Identify the blood parasite species.
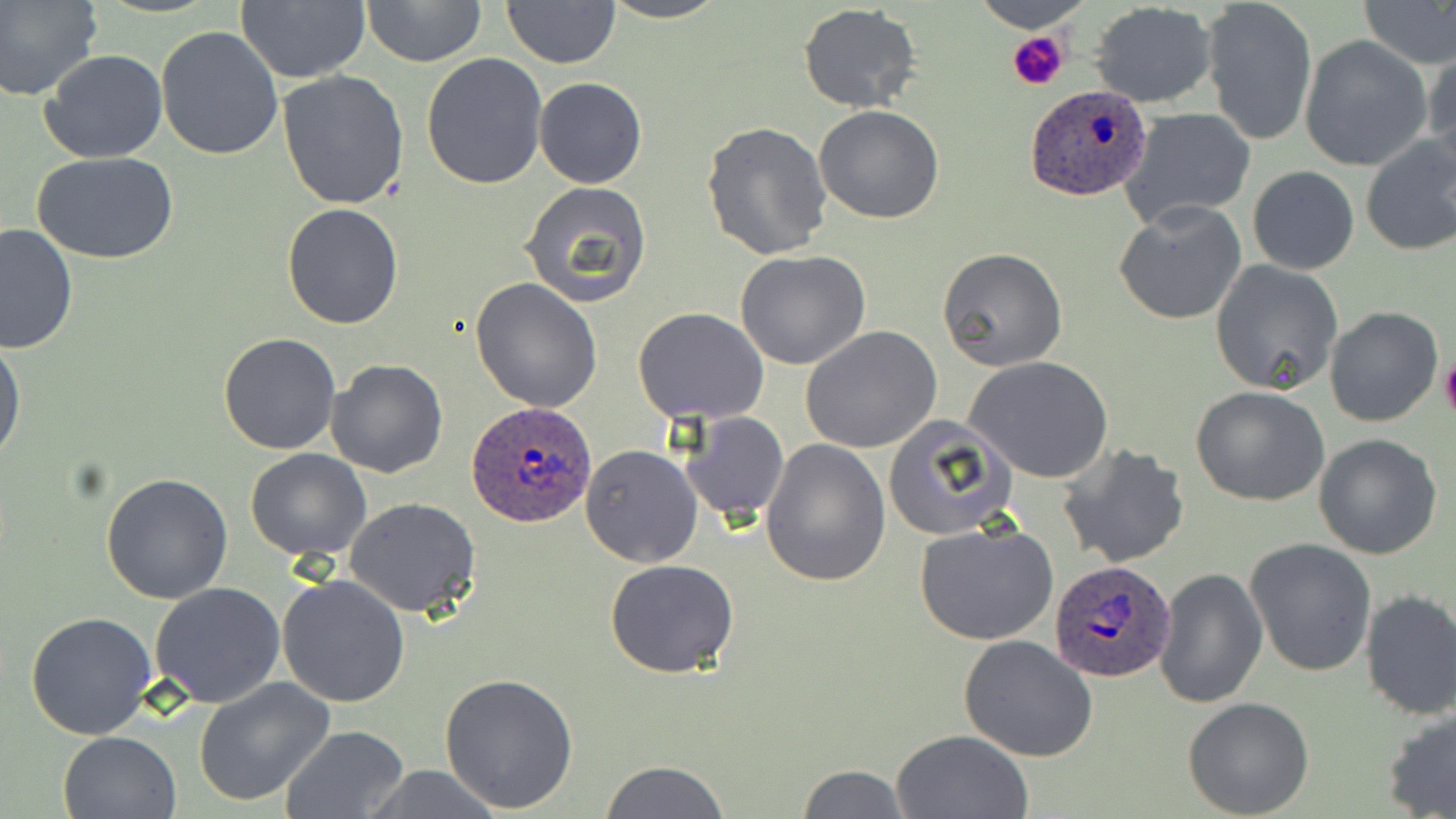
Plasmodium ovale.

Summary:
  - Coordinate format: approximate bounding boxes as (x1, y1, x2, y2) in pixels
  - Platelet locations: (1007, 32, 1071, 91), (1440, 359, 1456, 419)
  - Plasmodium ovale-infected red blood cell locations: (1025, 82, 1153, 199), (468, 401, 596, 528), (1050, 558, 1177, 683)
  - Uninfected red blood cell locations: (0, 0, 101, 102), (236, 0, 370, 84), (500, 0, 619, 68), (598, 0, 731, 24), (969, 0, 1095, 34), (1201, 0, 1317, 145), (362, 1, 486, 67), (1358, 1, 1456, 69), (1090, 2, 1216, 108), (797, 3, 923, 114), (155, 25, 285, 160), (1299, 36, 1433, 170), (40, 48, 168, 164), (1424, 49, 1456, 179), (421, 53, 548, 191), (278, 69, 410, 210), (534, 77, 646, 189), (814, 105, 946, 223), (1119, 108, 1257, 230), (701, 122, 832, 259), (1359, 135, 1456, 257), (32, 151, 180, 265), (1247, 164, 1359, 275), (519, 181, 653, 307), (1114, 201, 1247, 325), (281, 203, 405, 328), (1, 221, 78, 356), (938, 246, 1069, 372), (736, 249, 872, 369), (1211, 259, 1344, 396), (470, 277, 605, 412), (632, 306, 769, 425), (1323, 307, 1444, 428), (800, 326, 942, 453), (1, 331, 26, 471), (218, 333, 342, 454), (968, 357, 1113, 483), (325, 358, 449, 476), (1190, 385, 1330, 507), (678, 409, 789, 523), (883, 413, 1016, 542), (1313, 433, 1443, 558), (761, 438, 891, 585), (1058, 443, 1190, 569), (580, 445, 703, 567), (246, 449, 372, 561), (101, 473, 233, 604), (343, 497, 482, 620), (914, 519, 1060, 647), (1245, 538, 1378, 678), (605, 560, 739, 679), (1153, 568, 1267, 708), (277, 574, 411, 707), (150, 582, 286, 708), (1359, 588, 1456, 719), (26, 610, 158, 740), (958, 632, 1100, 761), (439, 672, 581, 814), (193, 677, 335, 807), (1182, 697, 1314, 818), (1380, 706, 1456, 818), (281, 725, 410, 819), (891, 729, 1033, 818), (57, 730, 182, 819), (602, 760, 730, 818), (795, 764, 910, 818), (355, 766, 509, 818)
  - Magnification: 1000x
  - Image size: 1456×819 pixels
  - Stain: May-Grünwald-Giemsa
  - Preparation: thin blood smear
  - Field of view: one of a larger specimen
  - Modality: optical microscopy